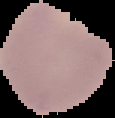

Summary:
  - Preparation: thin blood smear
  - Image size: 115×118 pixels
  - Malaria status: parasitized
  - Image type: segmented cell region on a black background